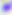 Micrograph. Toxoplasma gondii is shown. 400x magnification.